Report the malaria status of this cell.
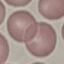

It is uninfected.

Photographed with a smartphone camera at the microscope eyepiece. Cell patch, automatically extracted from a larger field of view and resized to 64 × 64 pixels. Giemsa-stained preparation. Thin blood smear.